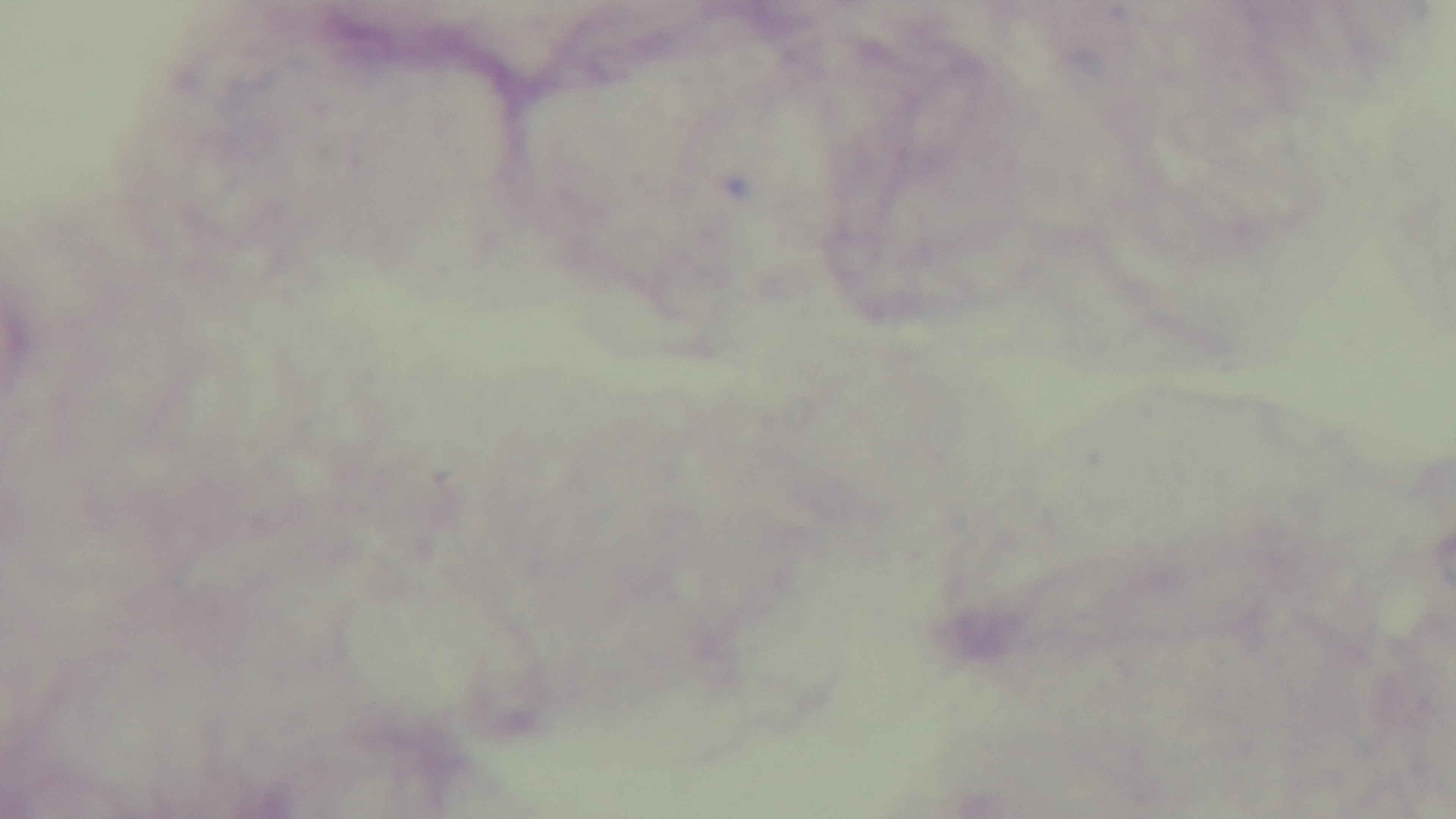

preparation: thick
field_of_view: one from the slide
capture: mounted 4K digital camera
objective: 100x oil immersion
modality: light microscopy
malaria_status: negative
stain: Giemsa